Mark where platelets are.
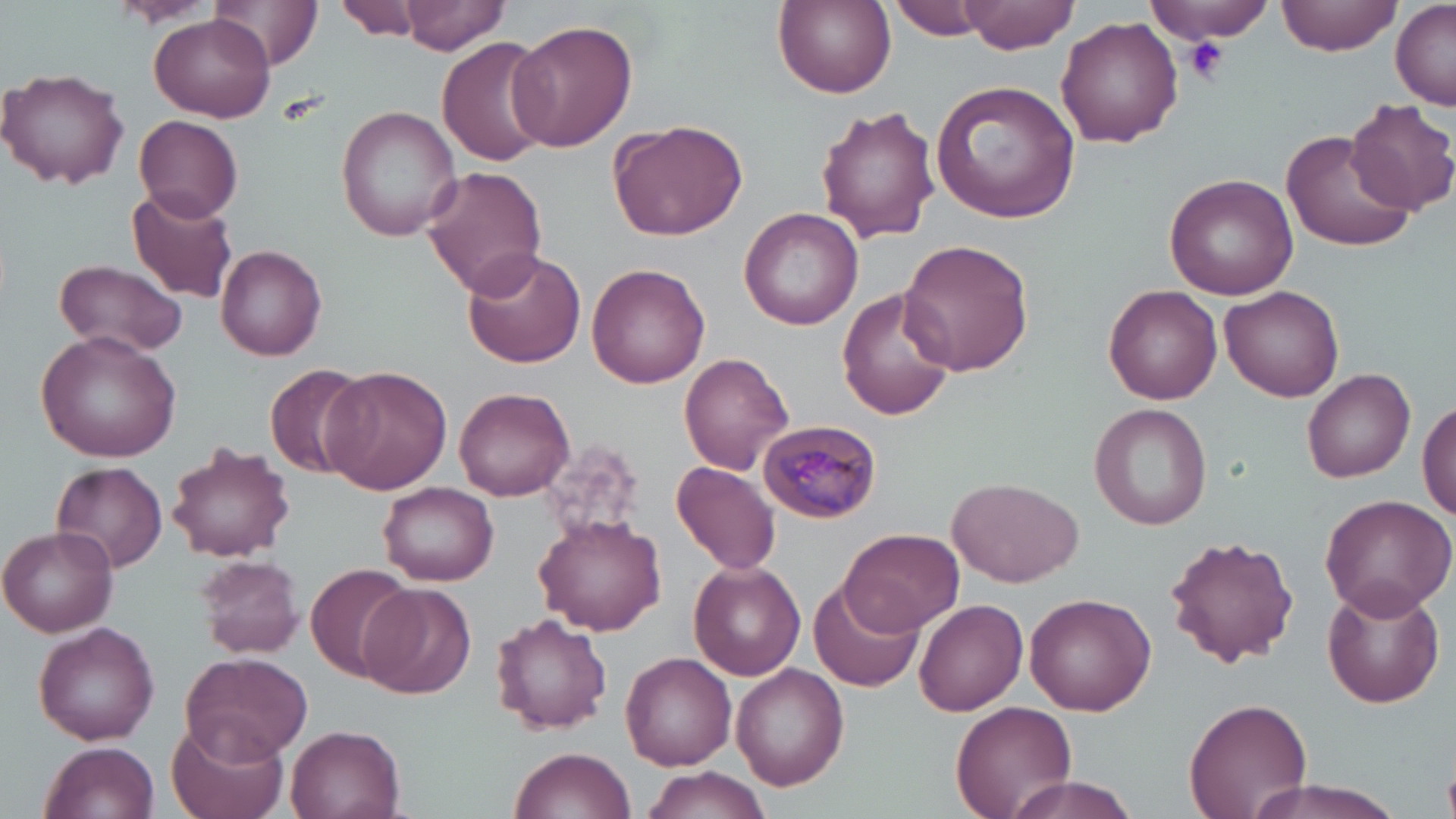
Approximate bounding boxes as (x1, y1, x2, y2) in pixels.
Platelets: (1184, 37, 1228, 84).

slide-level diagnosis = Plasmodium malariae
preparation = thin blood film
Plasmodium malariae-infected red blood cell locations = approximate bounding boxes as (x1, y1, x2, y2) in pixels: (758, 416, 882, 524)
field of view = one of a larger specimen
magnification = 1000x
uninfected red blood cell locations = approximate bounding boxes as (x1, y1, x2, y2) in pixels: (208, 0, 325, 70), (335, 0, 421, 42), (397, 0, 509, 54), (774, 0, 895, 98), (888, 0, 993, 40), (963, 0, 1081, 54), (1148, 0, 1273, 45), (1277, 0, 1402, 54), (1391, 0, 1455, 110), (103, 3, 224, 30), (148, 14, 277, 122), (1057, 15, 1183, 147), (506, 19, 638, 152), (436, 36, 554, 166), (1, 66, 130, 190), (930, 79, 1082, 224), (1344, 98, 1456, 216), (335, 104, 462, 241), (817, 104, 942, 245), (134, 113, 242, 224), (609, 117, 748, 242), (1281, 126, 1421, 255), (420, 166, 549, 297), (1164, 173, 1298, 300), (126, 188, 240, 304), (739, 206, 864, 330), (899, 239, 1033, 376), (216, 244, 327, 360), (461, 247, 584, 368), (53, 258, 188, 360), (586, 263, 710, 388), (837, 285, 957, 422), (1103, 285, 1222, 404), (1221, 286, 1345, 402), (35, 331, 183, 462), (678, 352, 794, 476), (265, 364, 369, 477), (320, 366, 452, 494), (1303, 367, 1415, 482), (455, 385, 575, 500), (1418, 395, 1456, 522), (1089, 402, 1213, 531), (540, 438, 649, 545), (166, 442, 295, 563), (49, 462, 171, 573), (670, 463, 782, 575), (946, 475, 1083, 587), (378, 481, 499, 585), (1319, 492, 1456, 617), (535, 516, 666, 636), (3, 528, 117, 636), (839, 528, 962, 635), (1163, 533, 1299, 666), (192, 554, 305, 659), (304, 562, 415, 683), (690, 562, 808, 682), (810, 579, 923, 694), (1322, 581, 1445, 708), (359, 583, 473, 697), (805, 591, 1027, 701), (1024, 593, 1156, 716), (915, 599, 1029, 714), (490, 613, 613, 734), (33, 621, 160, 745), (621, 652, 736, 768), (178, 653, 311, 763), (730, 663, 848, 790), (1183, 698, 1313, 819), (950, 700, 1076, 819), (167, 716, 289, 819), (286, 724, 406, 819), (39, 740, 160, 819), (509, 746, 634, 819), (641, 766, 771, 818), (1001, 773, 1140, 819), (1238, 776, 1416, 819)
modality = optical microscopy
image size = 1456×819 pixels
stain = May-Grünwald-Giemsa